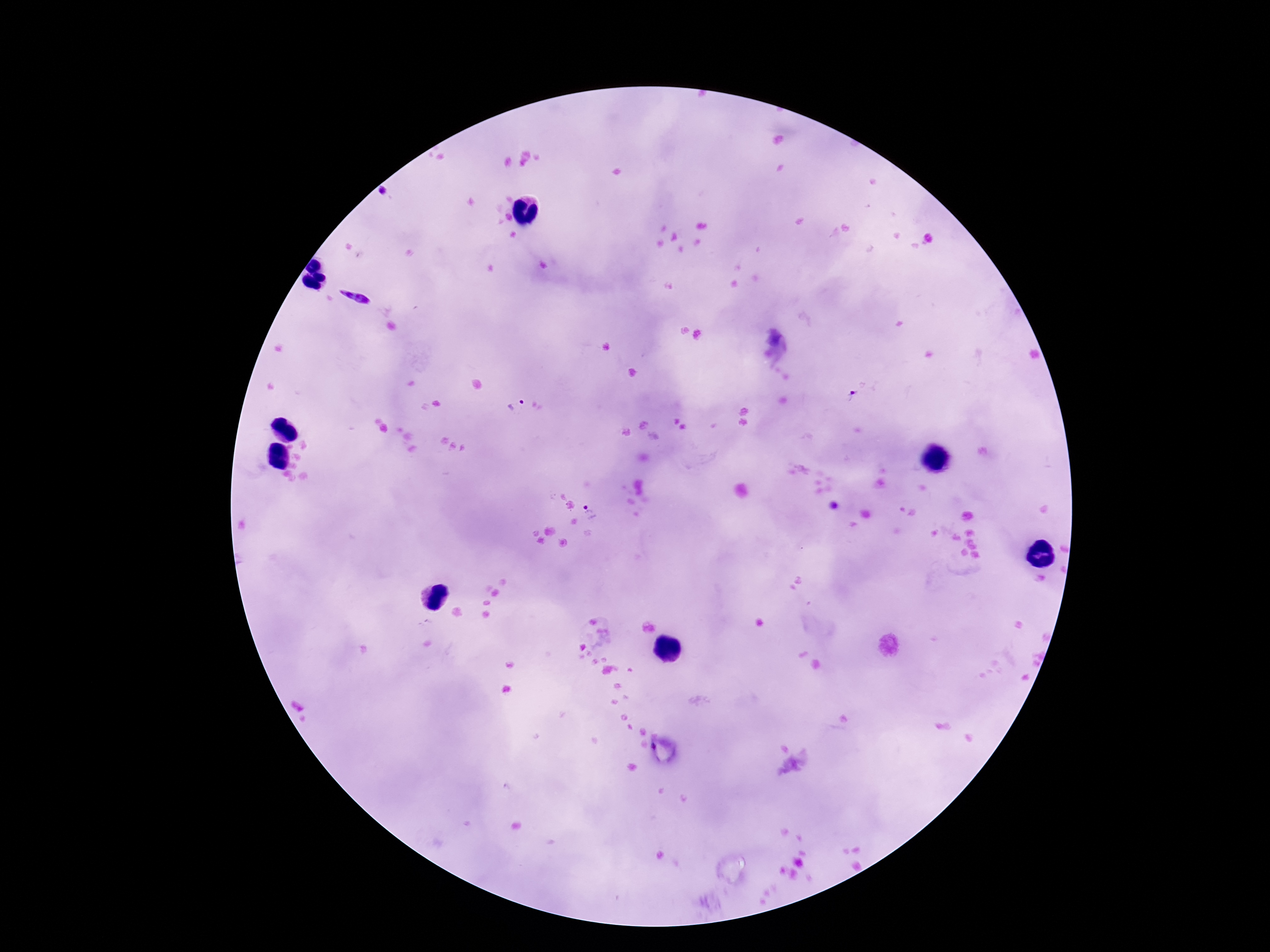
Approximate centers as {x, y} in pixels.
Summary:
  - Plasmodium parasite locations: {851, 394}, {516, 409}, {593, 513}
  - Image size: 1270×952 pixels
  - Field of view: one from this slide
  - Stain: Giemsa
  - Capture: smartphone camera through the microscope eyepiece
  - Magnification: 100x
  - Patient malaria status: positive
  - Preparation: thick blood film